Assess the morphology of the red blood cells.
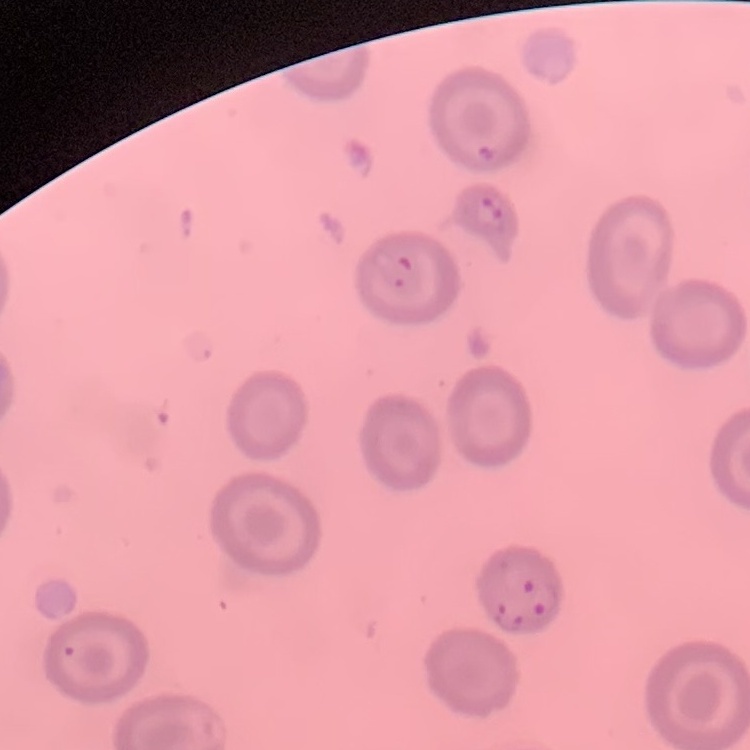

They show no rouleaux formation.

Square crop of a larger photomicrograph. Thin blood smear. Field's or Giemsa stain.